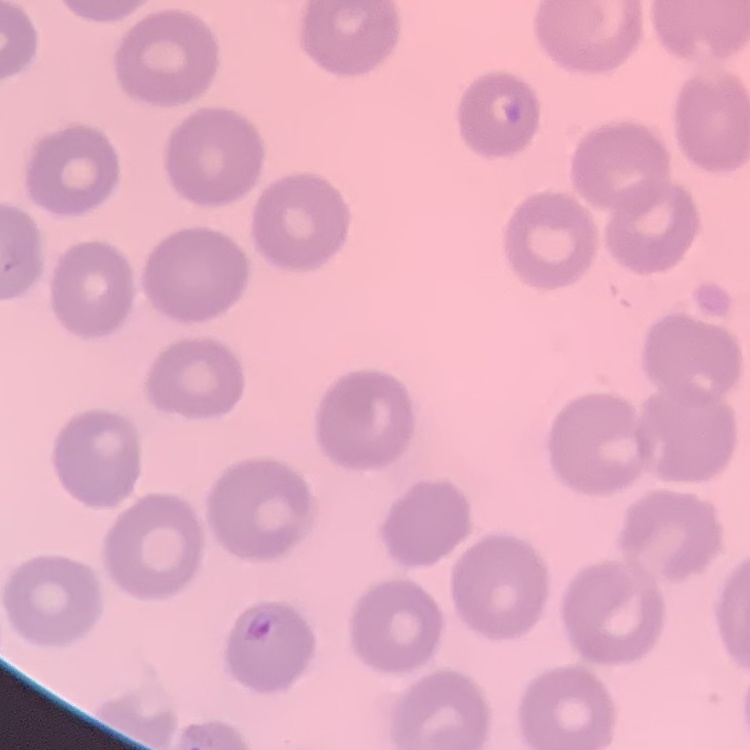

Summary:
  - Red blood cell morphology: no rouleaux formation
  - Image type: one tile cut from a larger photomicrograph
  - Stain: Field's or Giemsa
  - Preparation: thin blood film